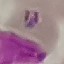
Summary:
  - Result: malaria parasites detected
  - Image type: automatically extracted cell patch, resized to 64 × 64 pixels
  - Stain: Giemsa
  - Capture: smartphone through the microscope eyepiece
  - Preparation: thin blood film